Assess the morphology of the red blood cells.
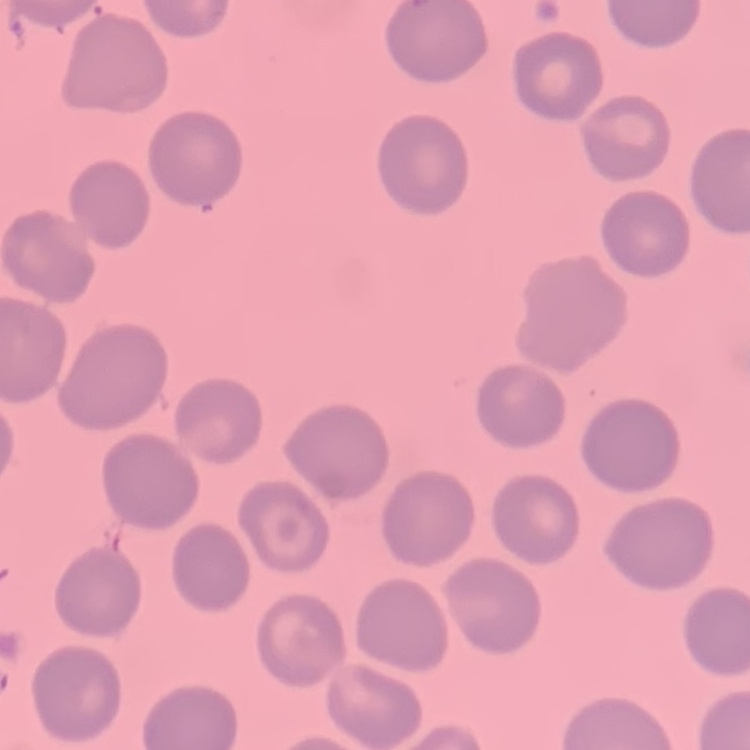

No rouleaux formation.

Thin blood smear. Stained with either Field's or Giemsa. One tile cut from a larger photomicrograph.